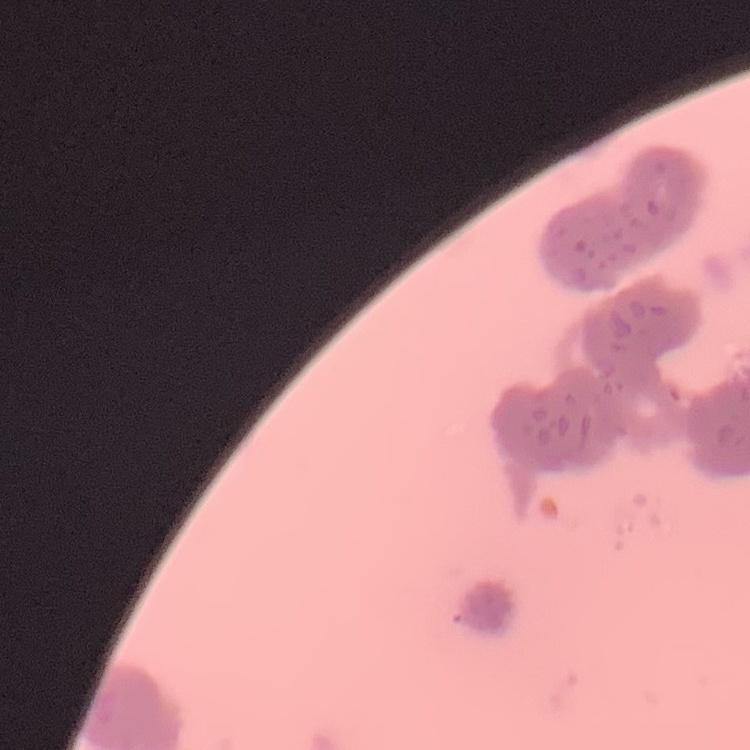
Summary:
  - Erythrocyte morphology: rouleaux formation
  - Preparation: thin blood film
  - Image type: square crop of a larger photomicrograph
  - Stain: Field's or Giemsa